Assess this cell for malaria.
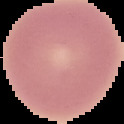
It is uninfected.

Image is 124×124 pixels. Cell region segmented out of the field of view; the surrounding area is masked to black. From a thin blood smear.